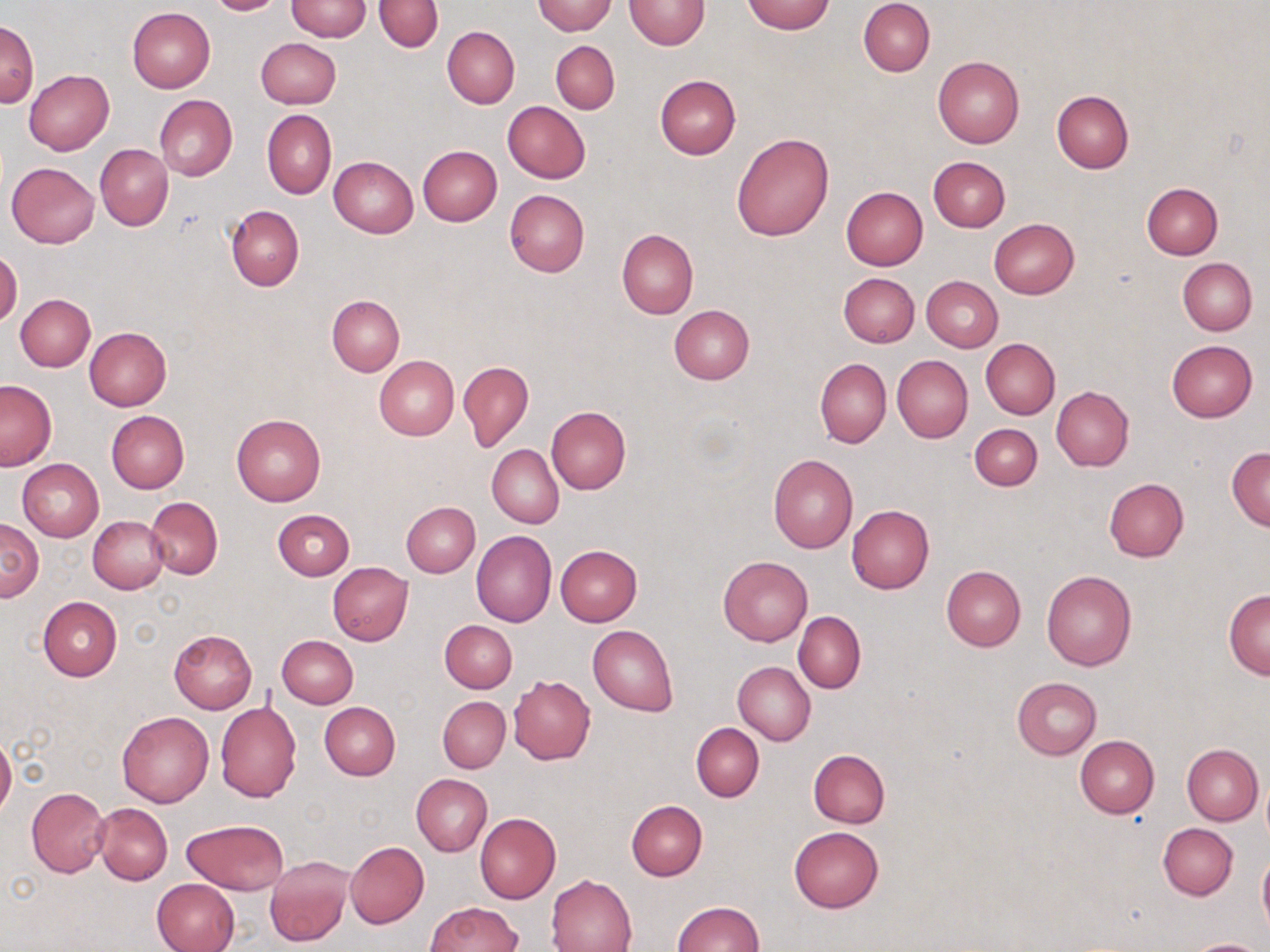
slide-level diagnosis = no evidence of blood parasites
image size = 1270×952 pixels
stain = May-Grünwald-Giemsa
field of view = one of a larger specimen
modality = light microscopy
magnification = 1000x
uninfected red blood cell locations = approximate bounding boxes as (x1, y1, x2, y2) in pixels: (206, 0, 286, 15), (374, 0, 443, 53), (625, 0, 710, 49), (859, 0, 935, 76), (285, 1, 373, 41), (531, 1, 616, 35), (742, 1, 835, 34), (127, 7, 215, 93), (0, 21, 39, 106), (442, 26, 519, 108), (255, 39, 341, 109), (551, 40, 620, 113), (932, 56, 1025, 147), (24, 69, 114, 154), (654, 75, 741, 159), (1051, 90, 1133, 173), (154, 95, 237, 181), (502, 101, 590, 183), (262, 109, 335, 199), (731, 131, 835, 241), (96, 144, 173, 230), (417, 146, 502, 226), (329, 156, 418, 237), (928, 156, 1010, 231), (5, 162, 99, 248), (1142, 183, 1222, 259), (841, 186, 928, 270), (504, 189, 590, 277), (226, 205, 304, 290), (989, 218, 1079, 298), (616, 229, 697, 319), (0, 250, 22, 327), (1178, 258, 1257, 335), (836, 272, 919, 347), (921, 276, 1003, 351), (15, 294, 95, 372), (327, 296, 405, 376), (668, 305, 754, 384), (85, 327, 171, 411), (980, 338, 1060, 418), (1165, 340, 1257, 423), (892, 355, 972, 442), (373, 356, 458, 441), (815, 358, 890, 448), (459, 361, 534, 452), (0, 379, 56, 471), (1051, 386, 1134, 471), (547, 406, 631, 495), (105, 410, 189, 494), (231, 413, 327, 507), (970, 423, 1043, 490), (487, 445, 564, 528), (1227, 446, 1270, 530), (769, 454, 858, 553), (17, 460, 103, 540), (1103, 478, 1188, 561), (145, 496, 223, 578), (401, 502, 479, 577), (847, 505, 935, 594), (274, 509, 354, 579), (88, 515, 169, 594), (0, 519, 42, 602), (471, 529, 556, 627), (556, 545, 642, 626), (718, 555, 812, 644), (328, 562, 413, 645), (942, 565, 1025, 651), (1041, 569, 1137, 671), (1223, 589, 1270, 679), (39, 596, 121, 681), (793, 611, 866, 693), (439, 620, 517, 693), (588, 624, 678, 717), (169, 629, 257, 712), (278, 635, 358, 709), (733, 661, 815, 746), (508, 676, 595, 764), (1011, 677, 1102, 759), (437, 696, 510, 773), (215, 701, 301, 802), (319, 702, 401, 780), (116, 711, 214, 808), (690, 722, 763, 802), (0, 733, 16, 820), (1074, 735, 1159, 818), (1182, 744, 1262, 825), (808, 749, 890, 827), (411, 773, 492, 856), (27, 786, 111, 877), (627, 800, 707, 880), (94, 803, 172, 884), (474, 812, 561, 904), (181, 819, 289, 894), (1158, 823, 1237, 900), (788, 827, 885, 912), (345, 842, 428, 927), (1258, 849, 1270, 937), (264, 856, 352, 947), (546, 874, 637, 952), (152, 878, 239, 952), (671, 901, 764, 952), (425, 902, 520, 951), (1180, 937, 1269, 952)
preparation = thin blood film